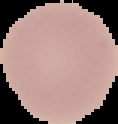
Summary:
  - Preparation: thin blood film
  - Image size: 118×124 pixels
  - Image type: segmented cell region with the area outside set to black
  - Result: negative for malaria parasites